Give the location of every parasitized RBC.
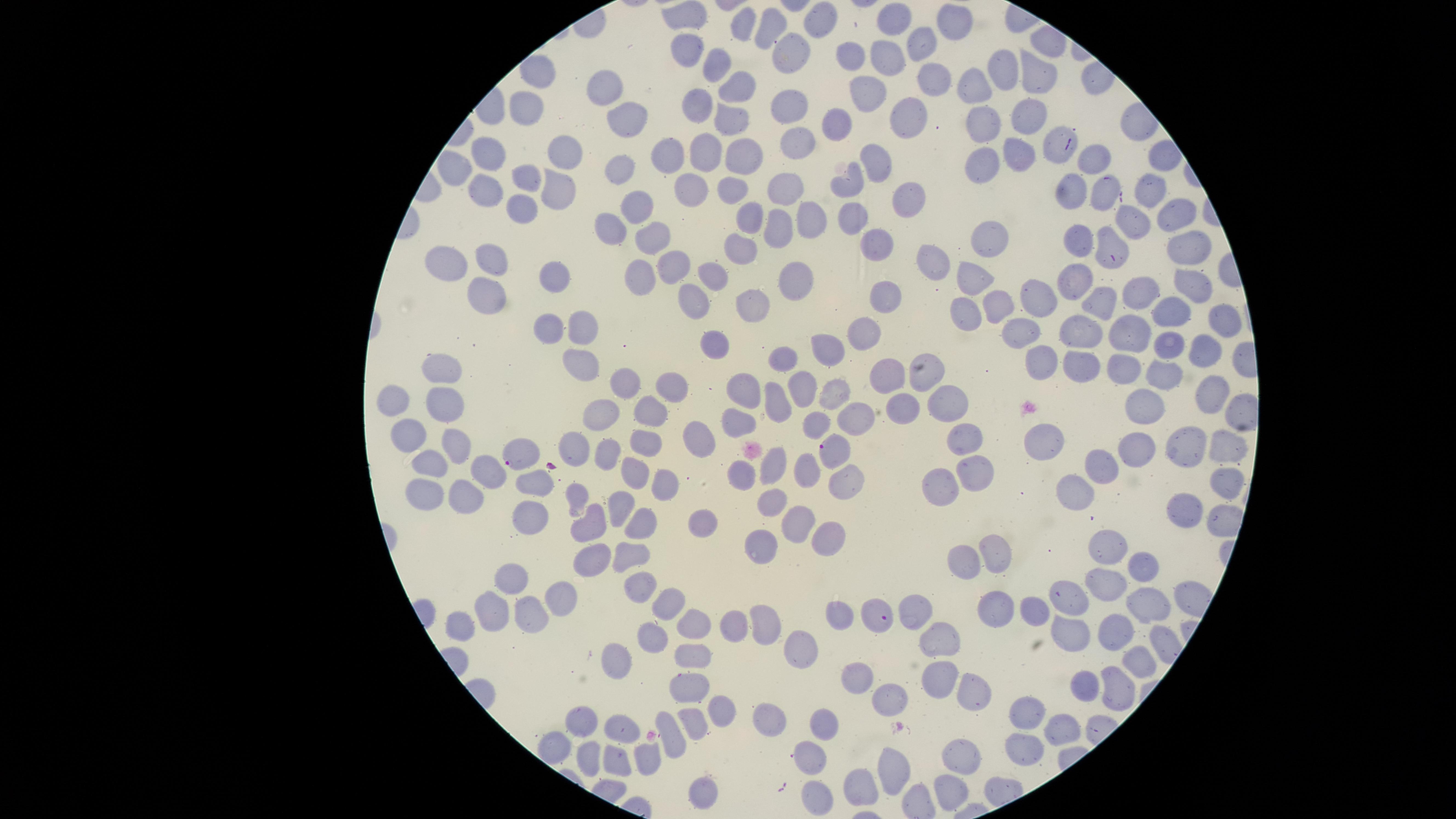
Approximate marker points as [x, y] in pixels.
Parasitized RBCs: [834, 450], [516, 454], [873, 613].

Approximate marker points as [x, y] in pixels.
Summary:
  - Uninfected RBCs: [688, 10], [813, 17], [891, 21], [954, 21], [746, 22], [773, 28], [922, 44], [685, 46], [788, 50], [856, 56], [884, 60], [718, 64], [1001, 69], [532, 70], [1036, 75], [934, 77], [739, 86], [972, 87], [606, 91], [870, 91], [701, 99], [788, 106], [524, 110], [1025, 113], [909, 116], [981, 117], [619, 119], [731, 122], [836, 126], [798, 132], [1054, 138], [566, 150], [707, 150], [672, 152], [490, 155], [1021, 155], [1096, 157], [880, 160], [743, 161], [981, 165], [454, 168], [622, 171], [526, 175], [855, 181], [556, 184], [688, 185], [784, 186], [1151, 186], [1076, 187], [731, 189], [488, 191], [1105, 192], [906, 194], [523, 202], [634, 202], [1172, 212], [855, 214], [755, 218], [809, 218], [780, 222], [1131, 223], [613, 226], [663, 234], [1111, 238], [875, 239], [994, 239], [1080, 239], [738, 247], [1183, 247], [672, 260], [486, 261], [933, 263], [448, 267], [713, 270], [553, 271], [975, 276], [1194, 277], [1073, 280], [647, 281], [792, 284], [1139, 289], [1041, 293], [1103, 293], [489, 295], [994, 301], [701, 303], [753, 303], [888, 303], [967, 308], [1168, 310], [1222, 318], [587, 322], [548, 325], [1083, 326], [1025, 328], [870, 330], [1127, 332], [721, 339], [1168, 340], [826, 348], [1210, 351], [584, 358], [1089, 359], [784, 360], [1039, 360], [1125, 364], [440, 368], [930, 374], [1162, 374], [887, 376], [629, 380], [671, 384], [805, 386], [748, 391], [837, 393], [1215, 395], [950, 397], [391, 402], [907, 402], [776, 404], [1150, 406], [651, 409], [442, 410], [607, 412], [850, 415], [736, 418], [817, 419], [408, 431], [965, 435], [696, 436], [573, 441], [1044, 444], [1189, 444], [643, 445], [1223, 445], [602, 448], [1133, 448], [420, 455], [455, 456], [1100, 463], [771, 465], [632, 470], [809, 470], [977, 470], [484, 471], [744, 473], [1223, 478], [849, 481], [536, 482], [427, 483], [944, 485], [663, 487], [1072, 489], [578, 492], [766, 495], [465, 498], [625, 499], [1188, 510], [527, 517], [795, 520], [588, 522], [640, 522], [698, 525], [825, 532], [759, 540], [1107, 540], [992, 546], [586, 556], [631, 557], [962, 562], [1138, 565], [510, 579], [636, 586], [1110, 586], [1071, 592], [555, 593], [668, 603], [1153, 604], [914, 609], [836, 610], [486, 616], [529, 617], [458, 621], [734, 621], [690, 625], [767, 625], [1122, 631], [1073, 635], [944, 637], [650, 638], [801, 642], [693, 651], [1137, 662], [610, 663], [862, 675], [696, 679], [941, 681], [1087, 683], [1114, 689], [969, 691], [888, 698], [1035, 705], [717, 708], [763, 714], [694, 717], [584, 721], [825, 722], [625, 724], [1064, 725], [670, 742], [1017, 742], [558, 744], [587, 754], [618, 755], [642, 755], [815, 756], [957, 763], [888, 768], [857, 789], [702, 790], [947, 791], [820, 799]
  - Capture: smartphone photograph through the microscope eyepiece
  - Species: Plasmodium falciparum
  - Stain: Giemsa
  - Image size: 1456×819 pixels
  - Visible region: circular
  - Field of view: single
  - Preparation: thin blood smear